Assess this cell for malaria.
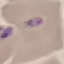

It is uninfected.

{
  "image_type": "cell patch, automatically extracted from a larger field of view and resized to 64 × 64 pixels",
  "stain": "Giemsa",
  "capture": "smartphone camera at the microscope eyepiece",
  "preparation": "thin blood film"
}